Report the malaria status of this cell.
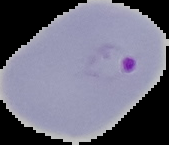

It is parasitized.

image_type: segmented cell region on a black background
preparation: thin blood film
image_size: 169×145 pixels